Assess the morphology of the erythrocytes.
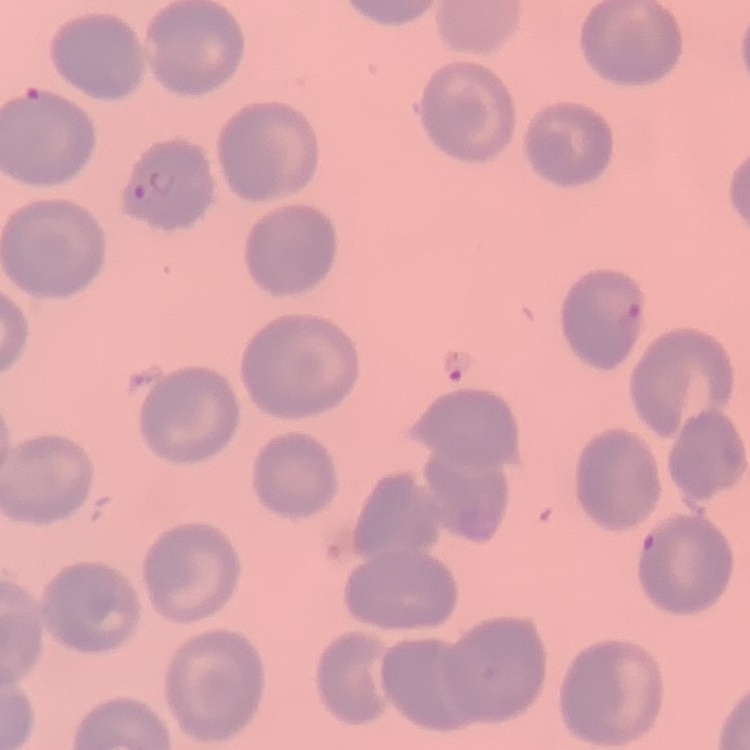
No rouleaux formation.

Stained with either Field's or Giemsa. Thin blood smear. Square crop of a larger photomicrograph.